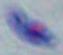
Summary:
  - Modality: micrograph
  - Magnification: 1000x
  - Identification: Toxoplasma gondii